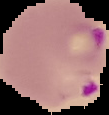

Summary:
  - Result: Plasmodium parasites detected
  - Image type: segmented cell region with the area outside set to black
  - Preparation: thin blood film
  - Image size: 109×115 pixels